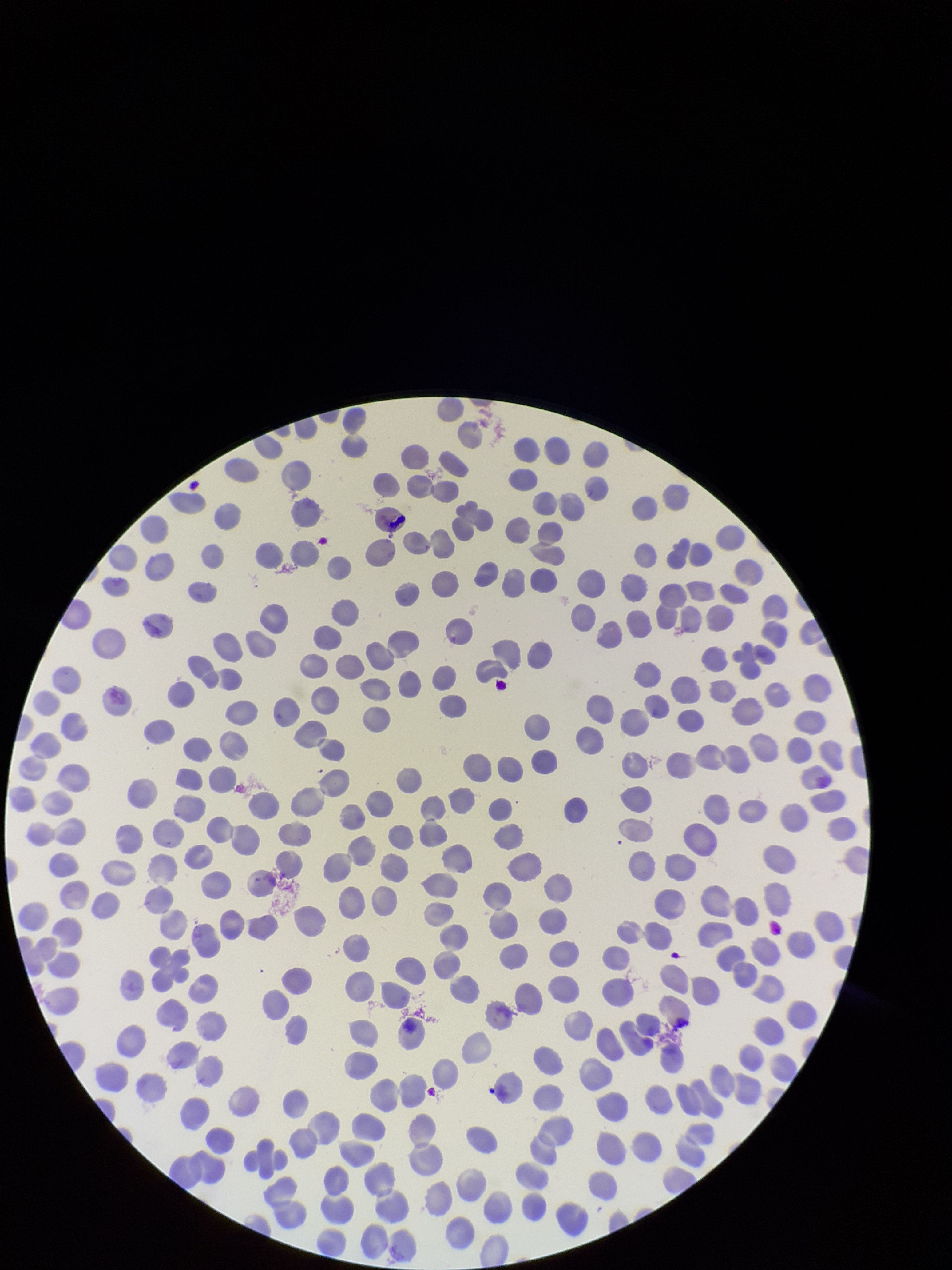
Summary:
  - Species reported for this patient: Plasmodium vivax
  - Patient malaria status: infected
  - Capture: smartphone photograph through the microscope eyepiece
  - Stain: Giemsa
  - Preparation: thin smear
  - Image size: 952×1270 pixels
  - Field of view: single
  - Parasitized red blood cell count: 0
  - Parasitized red blood cells: none identified
  - Red blood cell count: 310